Identify the blood parasite species.
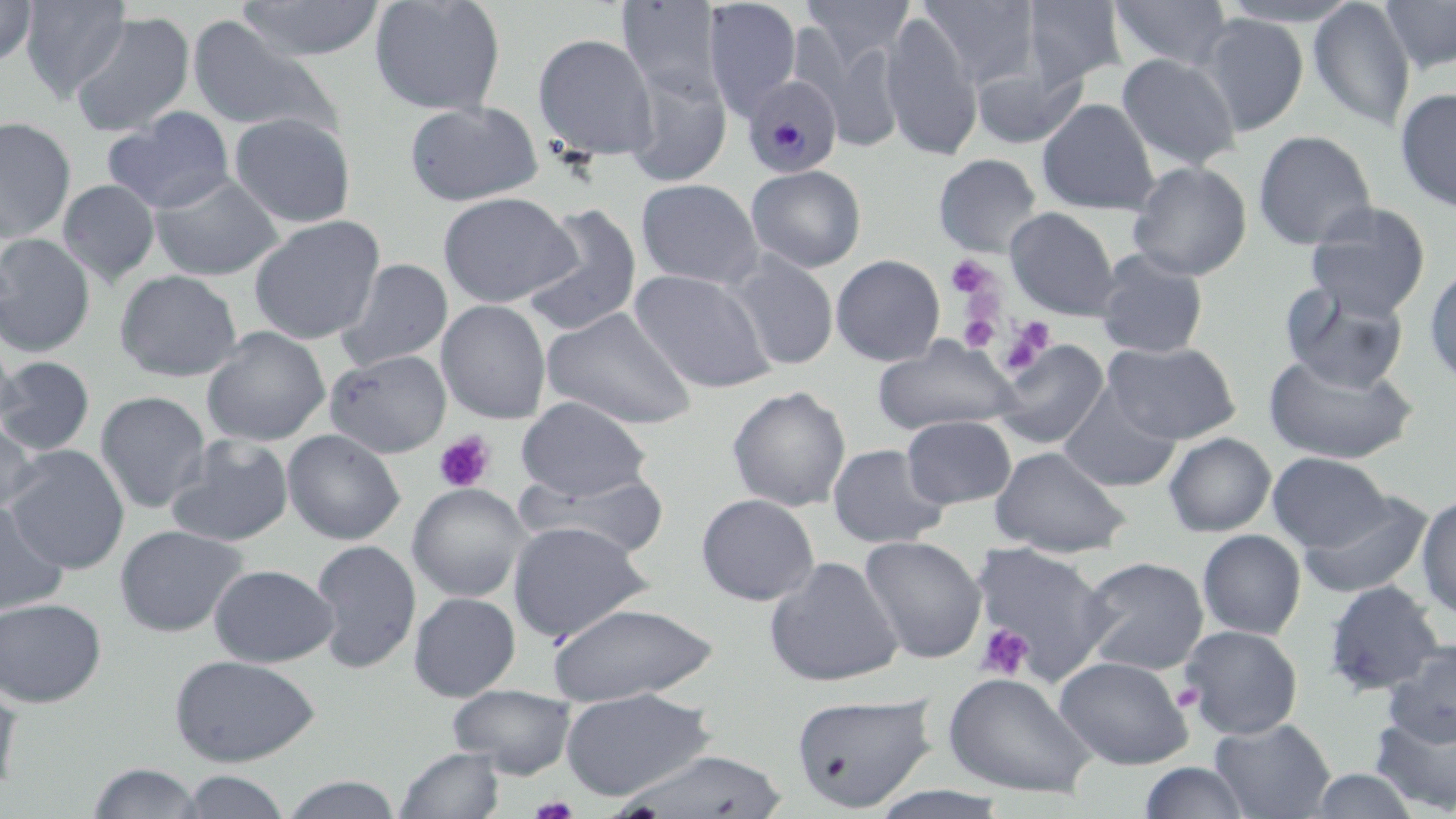
Plasmodium malariae.

Approximate bounding boxes as [x1, y1, x2, y2] in pixels. Platelet locations: [945, 256, 997, 301], [958, 312, 1001, 351], [1000, 316, 1057, 375], [433, 431, 496, 493], [975, 623, 1034, 681], [1173, 683, 1204, 712], [529, 795, 579, 818]. Uninfected red blood cell locations: [0, 0, 37, 66], [19, 0, 132, 102], [237, 0, 387, 62], [369, 0, 507, 116], [615, 0, 726, 104], [702, 0, 803, 118], [800, 0, 916, 71], [917, 0, 1042, 91], [1021, 0, 1127, 90], [1108, 0, 1234, 72], [1216, 0, 1367, 28], [1308, 0, 1416, 132], [1378, 0, 1456, 74], [880, 10, 983, 161], [69, 11, 195, 138], [1195, 14, 1309, 135], [187, 17, 344, 141], [532, 32, 659, 163], [805, 32, 909, 153], [1116, 54, 1241, 173], [970, 61, 1086, 149], [623, 70, 731, 187], [1395, 87, 1456, 213], [1037, 98, 1160, 214], [404, 101, 544, 206], [104, 108, 235, 215], [229, 113, 356, 228], [0, 116, 77, 243], [1253, 130, 1377, 250], [933, 153, 1043, 257], [1127, 161, 1252, 280], [745, 165, 867, 273], [150, 173, 284, 282], [635, 178, 764, 290], [58, 180, 160, 286], [437, 192, 579, 308], [1304, 202, 1431, 319], [520, 204, 644, 338], [1005, 207, 1120, 320], [249, 215, 385, 345], [0, 233, 96, 357], [1092, 249, 1210, 359], [725, 252, 840, 371], [831, 254, 945, 366], [335, 258, 453, 372], [1424, 260, 1456, 389], [630, 269, 778, 393], [115, 270, 242, 382], [1280, 283, 1409, 392], [436, 300, 552, 424], [541, 306, 699, 431], [202, 326, 330, 446], [0, 327, 17, 438], [872, 336, 1020, 436], [992, 338, 1110, 450], [1102, 340, 1242, 444], [325, 350, 451, 457], [1263, 351, 1418, 465], [0, 356, 96, 456], [727, 385, 851, 512], [1057, 385, 1181, 492], [95, 391, 211, 514], [515, 396, 653, 501], [902, 415, 1016, 508], [0, 419, 41, 516], [282, 428, 405, 545], [1163, 432, 1276, 537], [165, 434, 295, 547], [827, 443, 950, 548], [3, 445, 130, 574], [989, 445, 1132, 557], [1267, 451, 1393, 553], [514, 469, 671, 560], [407, 483, 531, 601], [1299, 492, 1433, 599], [696, 493, 820, 606], [1416, 494, 1456, 620], [0, 500, 68, 618], [507, 521, 652, 642], [114, 524, 248, 636], [1196, 529, 1306, 640], [860, 535, 988, 664], [310, 538, 421, 674], [970, 542, 1114, 684], [1078, 555, 1210, 675], [764, 556, 904, 688], [209, 563, 338, 667], [1322, 580, 1447, 697], [409, 592, 521, 701], [0, 597, 107, 707], [545, 602, 720, 705], [1179, 624, 1303, 739], [1383, 641, 1455, 747], [169, 654, 321, 766], [1053, 655, 1194, 770], [942, 671, 1098, 799], [0, 678, 22, 796], [447, 684, 577, 778], [559, 688, 716, 800], [791, 692, 936, 812], [1368, 709, 1456, 814], [1209, 717, 1336, 819], [395, 745, 505, 819], [612, 748, 793, 818], [1137, 761, 1254, 819], [86, 762, 207, 818], [1304, 768, 1424, 818], [177, 770, 293, 818], [277, 774, 405, 818], [864, 786, 1017, 819]. Plasmodium malariae-infected red blood cell locations: [742, 76, 842, 178]. Thin blood film. May-Grünwald-Giemsa stain. Single field of view. Optical microscopy. Image is 1456×819 pixels. Captured at 1000x magnification.